Locate every blood parasite and identify its species.
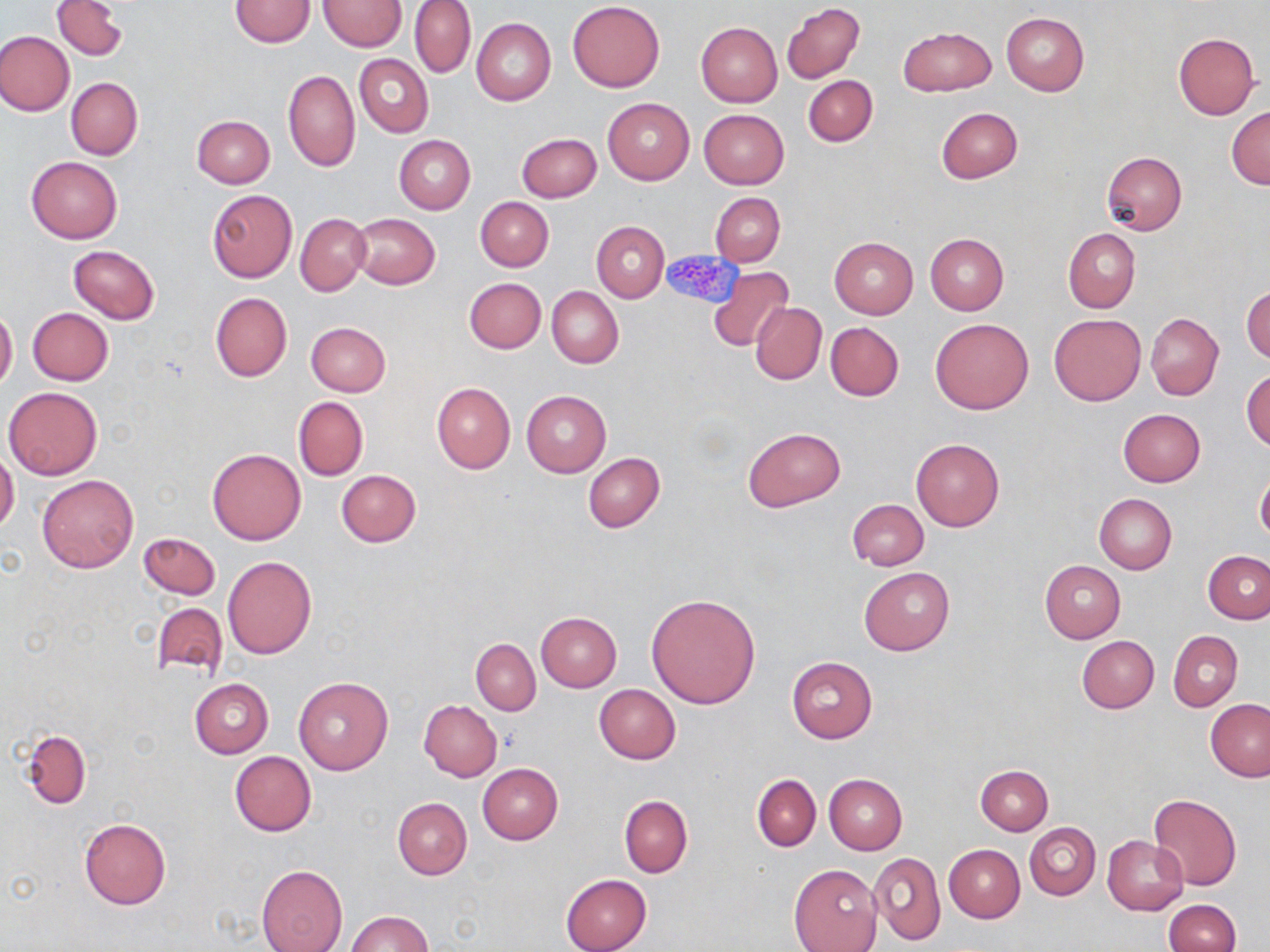

No blood parasites seen.

Approximate bounding boxes as (x1, y1, x2, y2) in pixels. Platelet locations: (660, 249, 744, 307). Uninfected red blood cell locations: (52, 0, 127, 60), (229, 0, 316, 46), (318, 0, 407, 50), (410, 0, 476, 78), (567, 1, 665, 92), (781, 2, 864, 85), (1001, 13, 1089, 95), (471, 17, 556, 105), (695, 21, 783, 106), (898, 25, 995, 94), (0, 30, 74, 116), (1173, 32, 1259, 119), (354, 54, 433, 136), (283, 70, 360, 172), (803, 74, 878, 147), (66, 77, 143, 159), (602, 98, 694, 184), (936, 107, 1021, 183), (1227, 107, 1269, 189), (698, 109, 789, 189), (192, 115, 275, 188), (516, 132, 601, 202), (394, 135, 475, 215), (1101, 151, 1187, 236), (26, 155, 123, 243), (207, 190, 296, 282), (710, 192, 786, 266), (475, 196, 554, 272), (296, 212, 370, 295), (350, 213, 439, 289), (592, 221, 669, 301), (1063, 228, 1140, 314), (925, 234, 1008, 315), (829, 237, 918, 319), (69, 245, 160, 323), (708, 266, 793, 353), (464, 278, 545, 353), (1242, 284, 1270, 364), (546, 287, 623, 368), (210, 292, 291, 382), (750, 302, 826, 385), (0, 306, 17, 391), (27, 307, 113, 385), (1145, 312, 1224, 399), (1050, 314, 1146, 406), (930, 319, 1033, 414), (825, 321, 904, 401), (306, 322, 391, 397), (1242, 370, 1270, 450), (432, 381, 515, 473), (4, 387, 103, 480), (521, 390, 610, 476), (294, 397, 367, 481), (1118, 408, 1206, 486), (743, 428, 845, 513), (911, 437, 1004, 532), (208, 448, 306, 545), (0, 451, 19, 532), (582, 452, 664, 532), (336, 469, 420, 547), (1256, 471, 1270, 545), (38, 473, 139, 573), (1093, 493, 1177, 574), (846, 499, 929, 571), (140, 532, 219, 600), (1203, 550, 1270, 624), (223, 556, 316, 659), (1040, 561, 1125, 643), (859, 566, 955, 656), (646, 593, 760, 709), (151, 603, 229, 679), (535, 612, 621, 692), (1168, 631, 1242, 710), (1076, 635, 1159, 713), (471, 639, 540, 715), (787, 656, 877, 743), (293, 676, 393, 775), (189, 679, 273, 757), (594, 685, 681, 764), (1205, 698, 1269, 782), (419, 701, 502, 781), (21, 729, 92, 808), (230, 751, 317, 835), (478, 763, 563, 845), (976, 764, 1053, 835), (824, 773, 907, 855), (752, 775, 821, 851), (1147, 793, 1241, 891), (619, 796, 693, 877), (393, 797, 472, 879), (78, 818, 171, 910), (1025, 823, 1099, 900), (1101, 835, 1188, 915), (943, 845, 1025, 922), (870, 852, 946, 946), (257, 864, 348, 952), (789, 864, 882, 952), (560, 874, 652, 952), (1163, 900, 1240, 952), (346, 911, 431, 952). Slide-level diagnosis: no evidence of blood parasites. Thin blood film. May-Grünwald-Giemsa stain. Optical microscopy. Image is 1270×952 pixels. 1000x magnification. Single field of view.